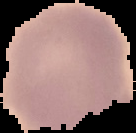
preparation = thin blood smear
result = no malaria parasites detected
image type = cell region segmented out of the field of view; surrounding area masked to black
image size = 136×133 pixels